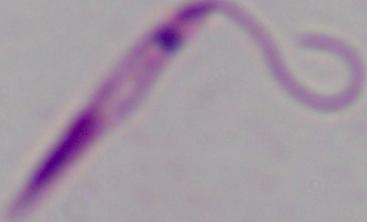

Summary:
  - Identification: Leishmania
  - Modality: micrograph
  - Magnification: 1000x